Locate every Plasmodium parasite.
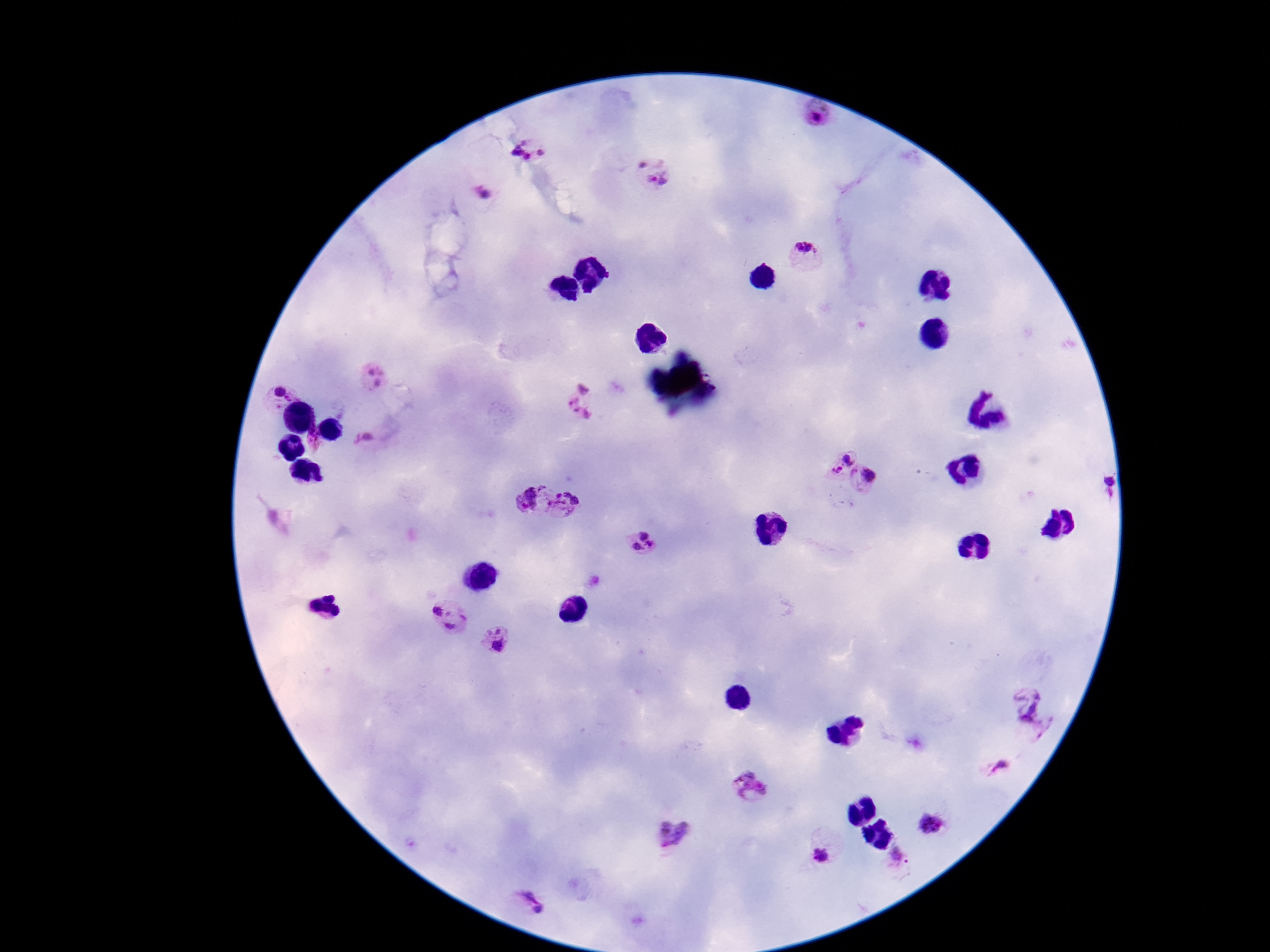
Approximate object centers, in pixels from the top-left corner.
Plasmodium parasites: (x=815, y=116), (x=520, y=152), (x=546, y=153), (x=647, y=156), (x=658, y=182), (x=482, y=193), (x=803, y=247), (x=374, y=377), (x=282, y=390), (x=582, y=404), (x=315, y=434), (x=366, y=440), (x=848, y=455), (x=838, y=472), (x=869, y=474), (x=1102, y=485), (x=532, y=499), (x=568, y=504), (x=644, y=543), (x=449, y=616), (x=495, y=638), (x=1035, y=713), (x=1000, y=771), (x=751, y=791), (x=930, y=823), (x=673, y=836), (x=820, y=854), (x=529, y=904).

Summary:
  - Stain: Giemsa
  - Preparation: thick peripheral-blood smear
  - Patient malaria status: infected
  - Capture: smartphone camera through the microscope eyepiece
  - Field of view: single
  - Magnification: 100x
  - Image size: 1270×952 pixels